Locate and identify every blood parasite.
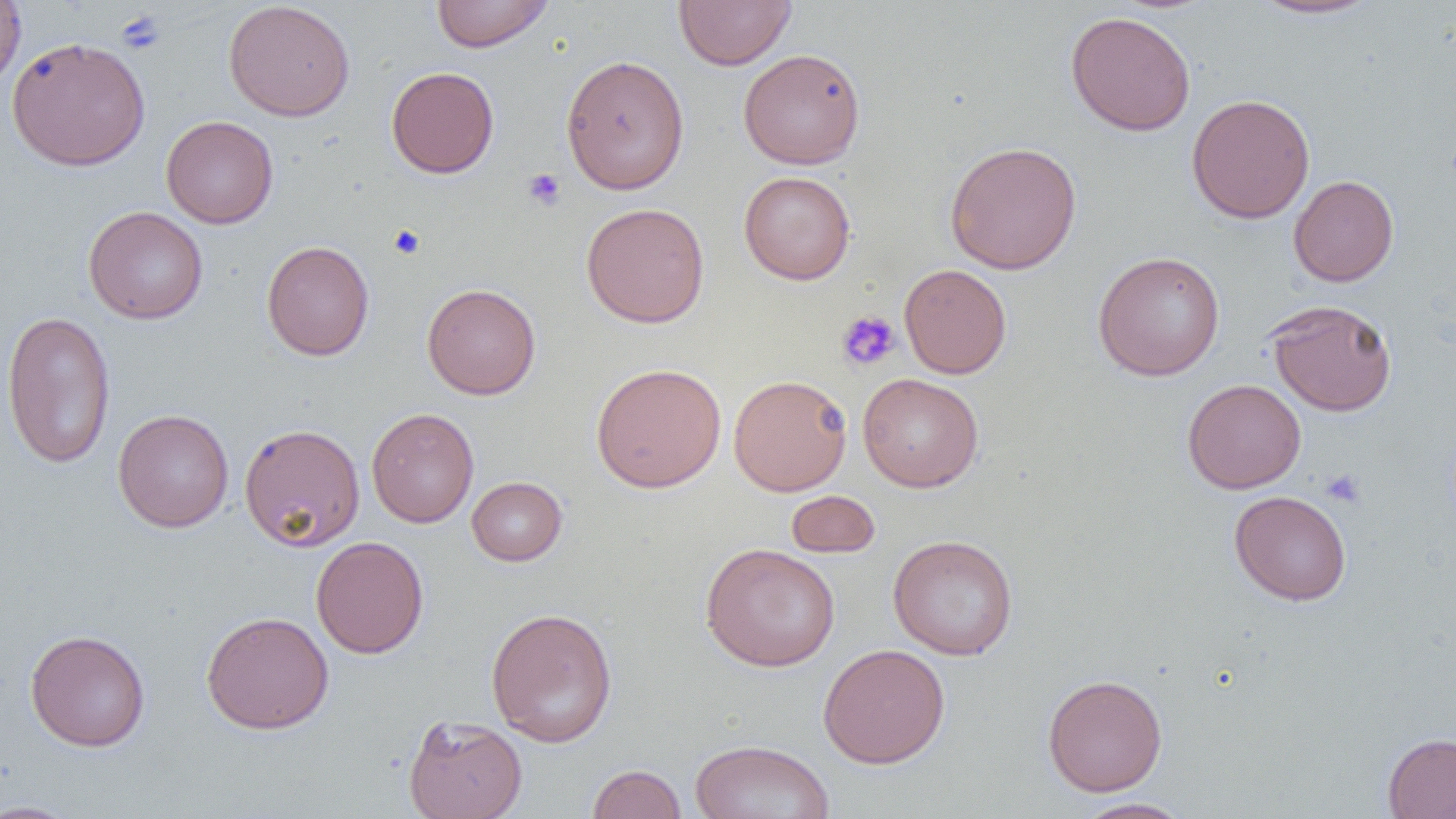

No blood parasites seen.

Approximate bounding boxes as (x1, y1, x2, y2) in pixels. Uninfected red blood cell locations: (0, 0, 26, 89), (430, 0, 554, 52), (673, 0, 797, 70), (1249, 0, 1382, 20), (223, 1, 355, 121), (1066, 10, 1196, 137), (7, 36, 150, 171), (738, 48, 866, 169), (560, 54, 690, 195), (386, 66, 499, 178), (1186, 93, 1315, 223), (161, 115, 278, 229), (944, 140, 1082, 275), (739, 170, 856, 285), (1289, 175, 1399, 287), (581, 202, 709, 328), (83, 206, 208, 324), (261, 240, 375, 361), (1093, 250, 1226, 381), (899, 263, 1012, 379), (422, 283, 541, 400), (1265, 299, 1397, 416), (1, 310, 116, 469), (591, 362, 727, 493), (858, 372, 984, 492), (728, 374, 852, 496), (1182, 379, 1306, 493), (366, 407, 479, 528), (113, 408, 234, 533), (238, 423, 366, 552), (466, 476, 567, 566), (785, 490, 881, 558), (1229, 490, 1351, 605), (888, 534, 1019, 660), (311, 536, 429, 659), (700, 542, 840, 672), (485, 606, 618, 747), (200, 610, 334, 734), (25, 629, 150, 752), (817, 643, 950, 768), (1042, 674, 1168, 796), (403, 714, 527, 819), (1383, 732, 1456, 819), (689, 739, 835, 819), (587, 764, 687, 818), (1072, 797, 1194, 819), (0, 800, 84, 818). Platelet locations: (116, 10, 166, 55), (522, 168, 566, 211), (388, 225, 426, 259), (836, 310, 901, 371), (1321, 469, 1366, 509). Slide-level diagnosis: negative for blood parasites. Image is 1456×819 pixels. Captured at 1000x magnification. Light microscopy. Thin blood smear. One field of a larger specimen.